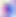
Summary:
  - Magnification: 400x
  - Modality: micrograph
  - Identification: Toxoplasma gondii